Name the parasite shown.
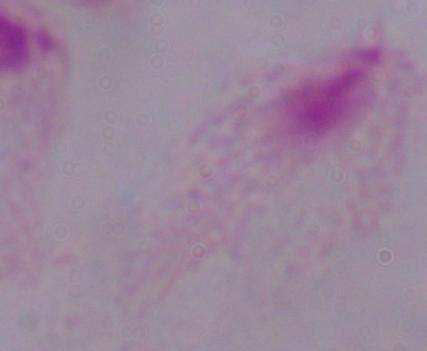
A trichomonad.

Summary:
  - Magnification: 1000x
  - Modality: photomicrograph